Assess the morphology of the erythrocytes.
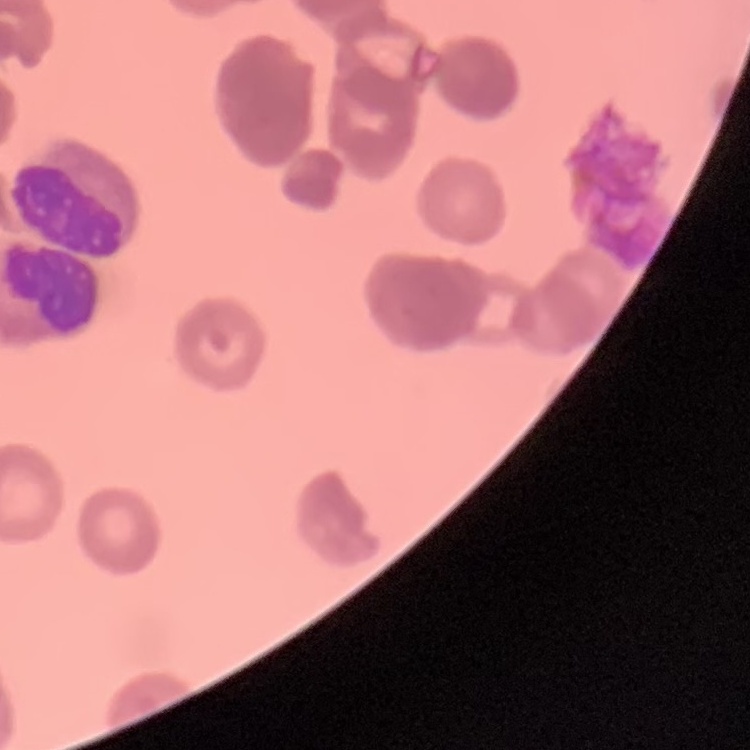
They show rouleaux formation.

Summary:
  - Preparation: thin blood film
  - Stain: Field's or Giemsa
  - Image type: square crop of a larger photomicrograph